Classify this cell by malaria status.
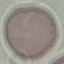
It is uninfected.

{
  "image_type": "automatically extracted cell patch, resized to 64 × 64 pixels",
  "stain": "Giemsa",
  "preparation": "thin smear",
  "capture": "smartphone through the microscope eyepiece"
}